Comment on the morphology of the erythrocytes.
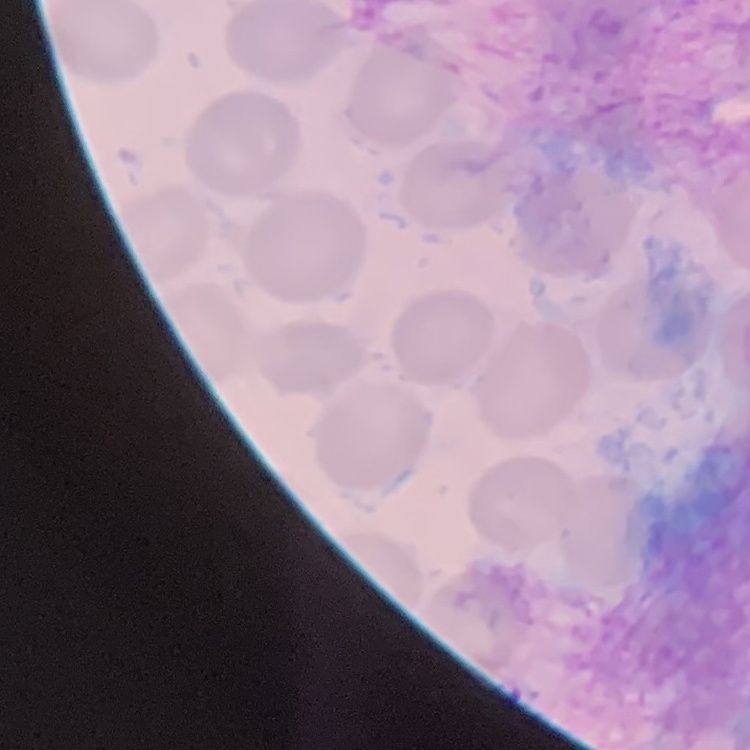
They show no rouleaux formation.

Summary:
  - Image type: square crop of a larger photomicrograph
  - Preparation: thin blood film
  - Stain: Field's or Giemsa